Give the extent of all Plasmodium falciparum-infected red blood cells.
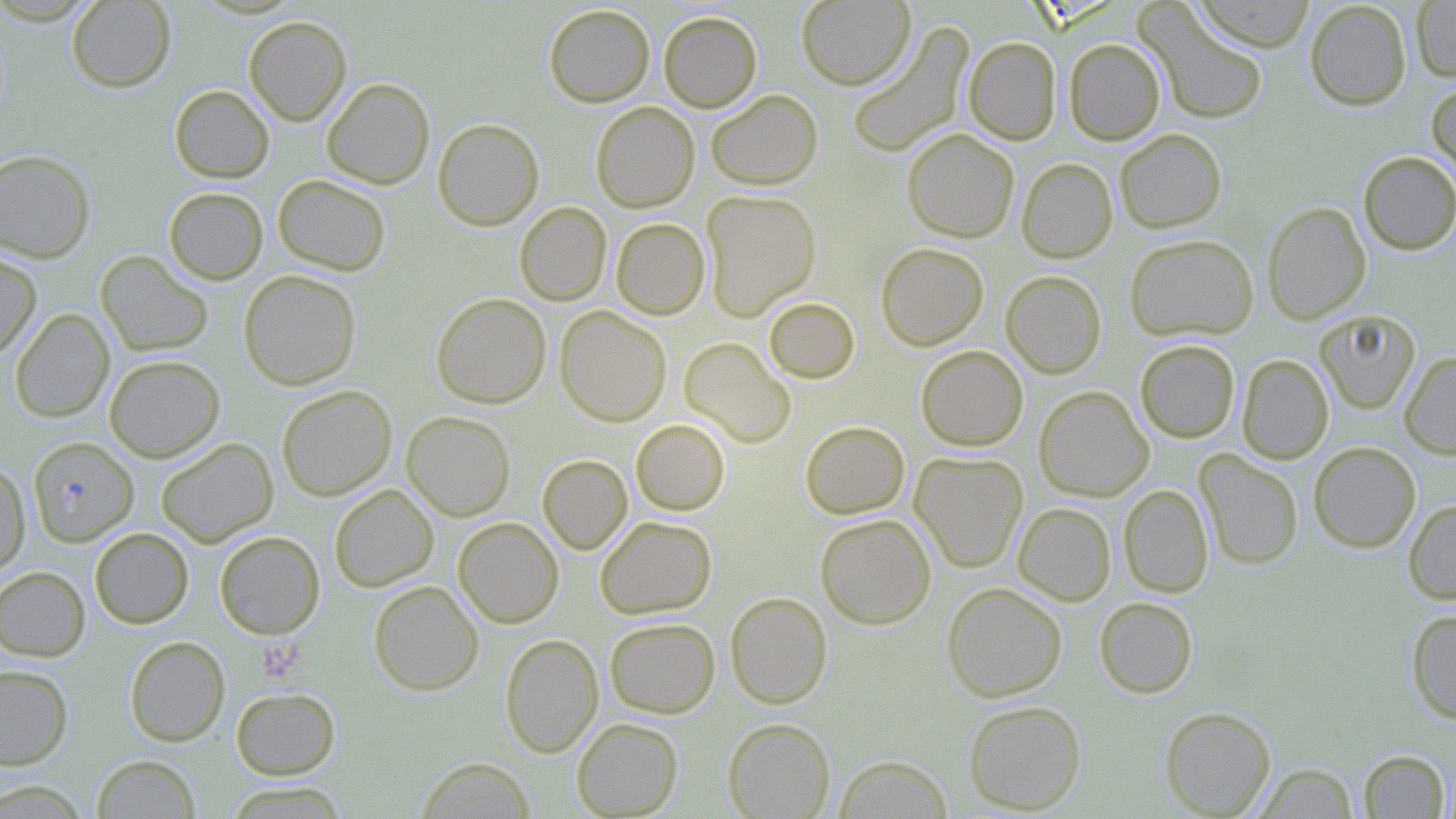
Approximate bounding boxes as [x1, y1, x2, y2] in pixels.
Plasmodium falciparum-infected red blood cells: [28, 437, 139, 545].

slide-level diagnosis = Plasmodium falciparum
magnification = 1000x
platelet locations = approximate bounding boxes as [x1, y1, x2, y2] in pixels: [258, 638, 305, 683]
preparation = thin blood smear
field of view = single
modality = light microscopy
uninfected red blood cell locations = approximate bounding boxes as [x1, y1, x2, y2] in pixels: [65, 0, 176, 92], [797, 0, 916, 91], [1191, 0, 1316, 52], [1304, 1, 1412, 110], [1410, 1, 1456, 82], [1135, 3, 1269, 125], [543, 4, 655, 107], [658, 10, 762, 112], [244, 16, 351, 125], [847, 23, 973, 157], [963, 37, 1062, 144], [1063, 38, 1165, 145], [321, 78, 434, 189], [1427, 80, 1456, 184], [169, 85, 274, 183], [705, 89, 823, 190], [590, 101, 699, 212], [433, 118, 544, 230], [901, 128, 1019, 243], [1115, 129, 1227, 233], [0, 149, 95, 263], [1358, 151, 1456, 255], [1016, 158, 1117, 263], [273, 175, 391, 275], [164, 187, 268, 285], [700, 189, 821, 320], [1262, 201, 1371, 324], [514, 202, 611, 306], [611, 218, 710, 320], [1124, 233, 1259, 342], [875, 242, 989, 350], [0, 250, 41, 361], [96, 251, 213, 356], [238, 270, 361, 390], [1000, 270, 1107, 378], [431, 293, 550, 409], [763, 297, 860, 383], [555, 306, 671, 426], [9, 308, 114, 423], [1314, 309, 1421, 414], [679, 337, 796, 448], [1135, 340, 1240, 442], [916, 345, 1028, 451], [1399, 351, 1456, 459], [1237, 354, 1333, 464], [104, 355, 225, 462], [276, 385, 396, 501], [1033, 385, 1153, 501], [402, 411, 515, 521], [631, 419, 730, 515], [800, 421, 910, 519], [155, 438, 278, 547], [1308, 442, 1420, 553], [1195, 449, 1303, 570], [910, 451, 1028, 573], [537, 454, 632, 554], [0, 462, 30, 576], [330, 484, 438, 592], [1119, 484, 1214, 598], [1403, 499, 1456, 605], [1013, 503, 1116, 606], [815, 514, 936, 629], [595, 516, 717, 619], [453, 518, 563, 628], [89, 527, 194, 629], [214, 531, 325, 639], [0, 566, 90, 661], [368, 580, 483, 695], [942, 582, 1067, 702], [725, 591, 832, 709], [1094, 596, 1198, 698], [1406, 608, 1456, 724], [605, 617, 719, 718], [499, 633, 603, 758], [124, 636, 230, 747], [0, 665, 73, 769], [230, 687, 340, 780], [963, 699, 1087, 814], [1160, 706, 1276, 818], [572, 717, 683, 817], [722, 717, 835, 818], [1358, 749, 1450, 818], [92, 754, 200, 818], [835, 754, 952, 818], [415, 756, 536, 818], [1254, 761, 1360, 818], [0, 779, 92, 818], [222, 781, 351, 818]
stain = May-Grünwald-Giemsa
image size = 1456×819 pixels